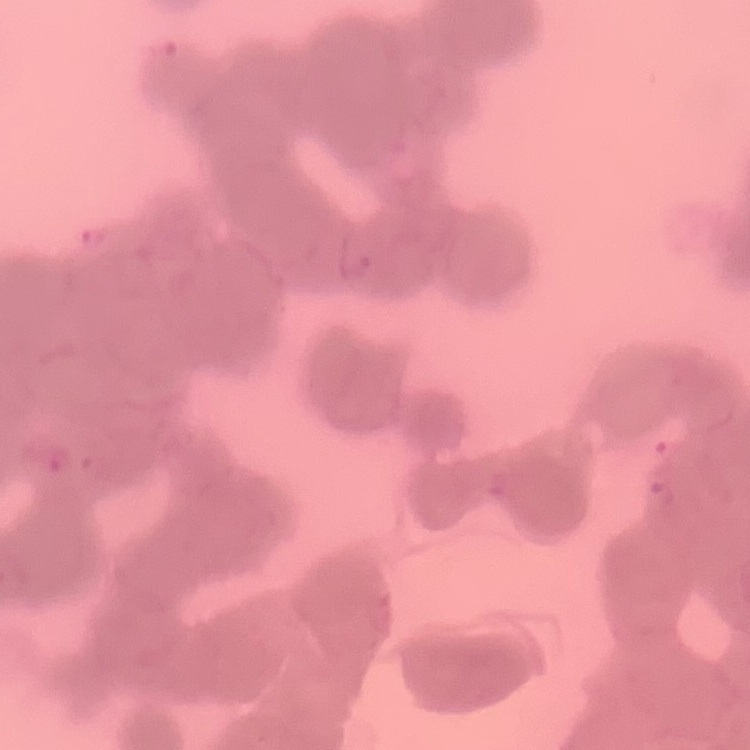

The red blood cells show rouleaux formation. One tile cut from a larger photomicrograph. Thin blood smear. Field's or Giemsa stain.